Report the malaria status of this cell.
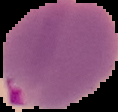

It is parasitized.

Summary:
  - Image size: 118×112 pixels
  - Preparation: thin blood smear
  - Image type: segmented cell region with the area outside set to black